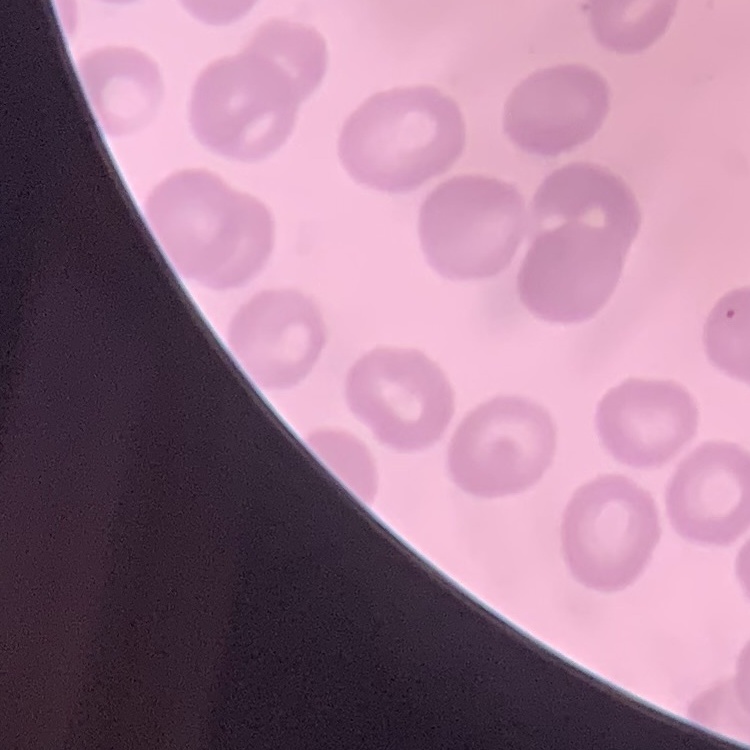
Summary:
  - Red blood cell morphology: no rouleaux formation
  - Stain: Field's or Giemsa
  - Preparation: thin peripheral smear
  - Image type: square crop of a larger photomicrograph